Assess this cell for malaria.
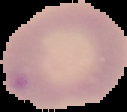

Parasitized.

Segmented cell region on a black background. From a thin blood smear. Image is 127×112 pixels.